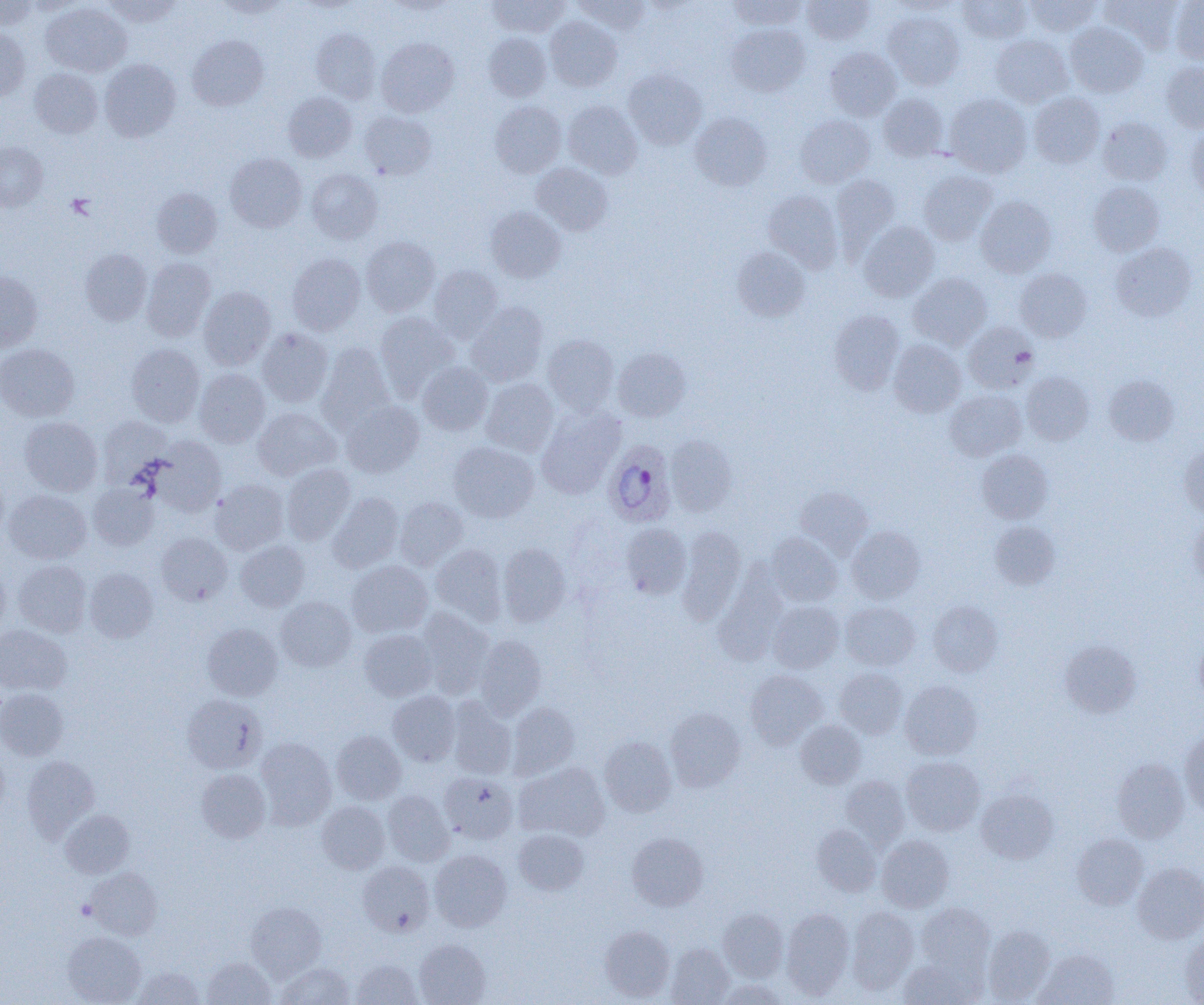
{
  "slide_level_diagnosis": "Plasmodium ovale",
  "field_of_view": "single",
  "modality": "light microscopy",
  "uninfected_red_blood_cell_locations": "approximate bounding boxes as [x1, y1, x2, y2] in pixels: [103, 0, 181, 26], [214, 0, 293, 18], [486, 0, 569, 37], [573, 0, 650, 34], [729, 0, 808, 29], [802, 0, 875, 44], [958, 0, 1033, 43], [1025, 0, 1101, 37], [1101, 0, 1183, 50], [0, 1, 37, 30], [21, 1, 85, 15], [385, 1, 455, 16], [889, 1, 962, 16], [1169, 1, 1204, 64], [41, 2, 132, 77], [883, 12, 964, 90], [545, 17, 622, 91], [1065, 22, 1148, 97], [726, 24, 810, 96], [0, 28, 30, 103], [310, 29, 381, 103], [484, 32, 551, 101], [187, 35, 268, 111], [990, 35, 1072, 107], [377, 37, 459, 117], [825, 47, 901, 120], [99, 59, 181, 142], [1162, 61, 1204, 132], [29, 68, 103, 138], [623, 68, 707, 149], [283, 92, 357, 162], [878, 93, 949, 161], [944, 93, 1032, 178], [1029, 93, 1104, 168], [562, 100, 642, 178], [490, 101, 566, 177], [359, 111, 437, 180], [690, 112, 772, 191], [795, 115, 875, 187], [1097, 116, 1172, 185], [1186, 127, 1204, 201], [0, 142, 48, 211], [225, 152, 307, 232], [531, 163, 613, 235], [306, 168, 383, 244], [918, 170, 997, 245], [831, 174, 900, 254], [1088, 181, 1164, 256], [151, 188, 221, 258], [763, 190, 843, 272], [975, 195, 1056, 277], [485, 206, 566, 282], [859, 222, 939, 301], [361, 237, 440, 316], [1111, 243, 1197, 322], [732, 246, 810, 321], [80, 248, 152, 325], [287, 253, 365, 335], [141, 257, 215, 341], [429, 265, 503, 343], [1015, 268, 1092, 342], [0, 270, 42, 351], [908, 272, 992, 350], [198, 287, 276, 369], [466, 302, 548, 386], [829, 309, 905, 395], [375, 311, 458, 397], [964, 322, 1038, 393], [257, 328, 333, 407], [543, 334, 619, 414], [888, 339, 966, 417], [317, 343, 394, 431], [0, 344, 80, 421], [126, 344, 204, 426], [613, 347, 691, 421], [418, 362, 493, 435], [194, 369, 270, 447], [1021, 371, 1093, 445], [1104, 374, 1179, 446], [481, 378, 559, 457], [945, 390, 1026, 461], [340, 400, 424, 477], [536, 406, 625, 498], [252, 407, 341, 481], [98, 416, 172, 485], [19, 417, 103, 495], [665, 435, 737, 516], [150, 437, 226, 516], [448, 441, 539, 522], [1179, 445, 1204, 516], [977, 449, 1053, 523], [281, 464, 355, 545], [0, 470, 9, 541], [210, 480, 288, 554], [87, 483, 158, 551], [795, 486, 872, 556], [4, 489, 91, 564], [328, 492, 404, 573], [395, 497, 468, 570], [1188, 517, 1204, 592], [989, 520, 1060, 590], [621, 523, 691, 599], [678, 526, 746, 623], [847, 526, 925, 604], [156, 532, 233, 605], [766, 533, 843, 606], [235, 540, 309, 612], [497, 543, 570, 626], [431, 544, 507, 625], [13, 560, 91, 637], [347, 561, 433, 637], [0, 565, 10, 637], [713, 567, 788, 665], [84, 568, 158, 642], [276, 596, 356, 671], [768, 600, 844, 673], [840, 601, 920, 670], [928, 601, 1002, 677], [417, 609, 495, 698], [203, 623, 282, 700], [0, 625, 71, 694], [359, 629, 437, 700], [474, 634, 546, 719], [1194, 637, 1204, 704], [1059, 639, 1142, 718], [835, 667, 908, 739], [745, 670, 826, 748], [900, 681, 982, 759], [0, 688, 68, 760], [387, 691, 460, 767], [182, 694, 267, 774], [446, 698, 516, 780], [508, 702, 579, 779], [665, 707, 745, 792], [796, 720, 866, 788], [1180, 729, 1204, 816], [331, 730, 406, 804], [599, 736, 677, 816], [255, 737, 336, 828], [0, 747, 10, 821], [22, 755, 99, 841], [901, 756, 985, 835], [1112, 758, 1189, 842], [514, 762, 609, 842], [196, 769, 271, 842], [439, 773, 517, 843], [841, 776, 909, 848], [976, 789, 1058, 864], [383, 790, 454, 865], [317, 801, 390, 873], [61, 809, 135, 878], [812, 824, 881, 896], [513, 829, 589, 896], [627, 832, 709, 910], [1072, 834, 1148, 909], [877, 835, 954, 912], [429, 849, 511, 931], [357, 860, 434, 936], [1133, 863, 1204, 942], [87, 867, 162, 939], [246, 902, 326, 981], [916, 903, 995, 975], [847, 906, 919, 992], [718, 908, 788, 981], [781, 908, 854, 998], [600, 925, 674, 1001], [983, 925, 1055, 1003], [62, 931, 146, 1005], [1181, 933, 1204, 1004], [414, 939, 491, 1005], [666, 943, 734, 1004], [1034, 949, 1118, 1005], [202, 956, 276, 1004], [899, 957, 981, 1005], [351, 958, 422, 1005], [276, 962, 354, 1004], [131, 967, 204, 1004], [717, 979, 790, 1005]",
  "image_size": "1204×1005 pixels",
  "preparation": "thin blood film",
  "platelet_locations": "approximate bounding boxes as [x1, y1, x2, y2] in pixels: [67, 194, 96, 218], [76, 899, 97, 920]",
  "plasmodium_ovale_infected_red_blood_cell_locations": "approximate bounding boxes as [x1, y1, x2, y2] in pixels: [603, 440, 677, 527]",
  "magnification": "1000x"
}